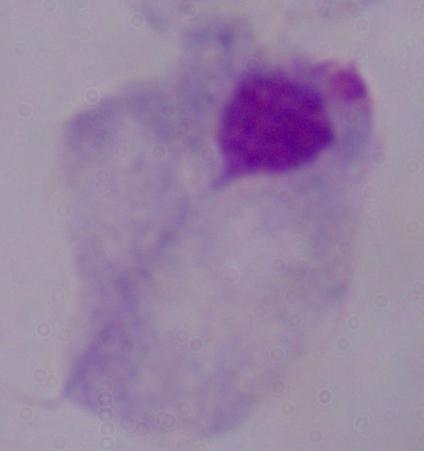

magnification = 1000x
modality = micrograph
identification = trichomonad